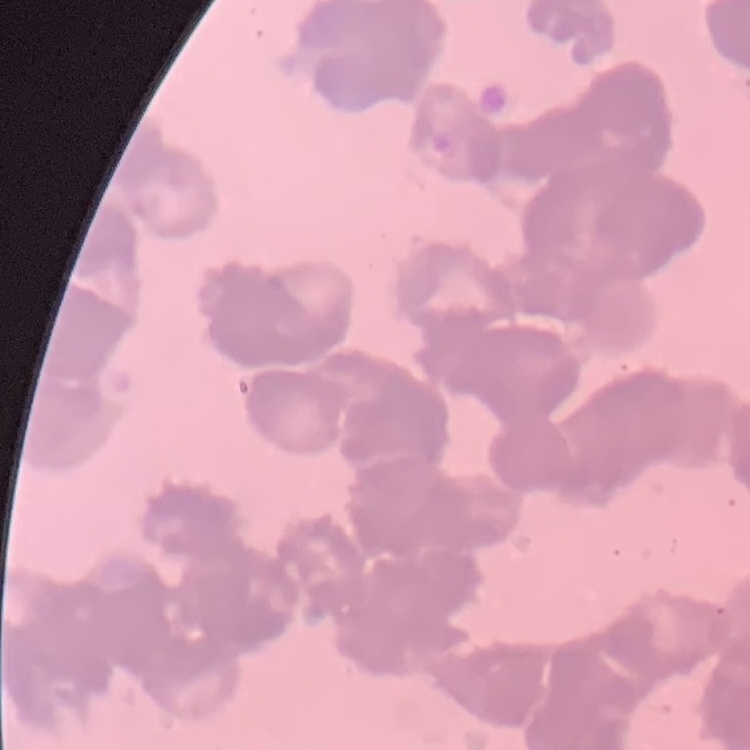
red blood cell morphology = rouleaux formation
image type = square crop of a larger photomicrograph
stain = Field's or Giemsa
preparation = thin peripheral smear